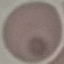
result = negative for malaria parasites
image type = cell patch, automatically extracted from a larger field of view and resized to 64 × 64 pixels
stain = Giemsa
preparation = thin blood film
capture = smartphone camera at the microscope eyepiece